State which parasite is depicted.
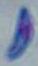
Toxoplasma gondii.

modality: micrograph
magnification: 1000x